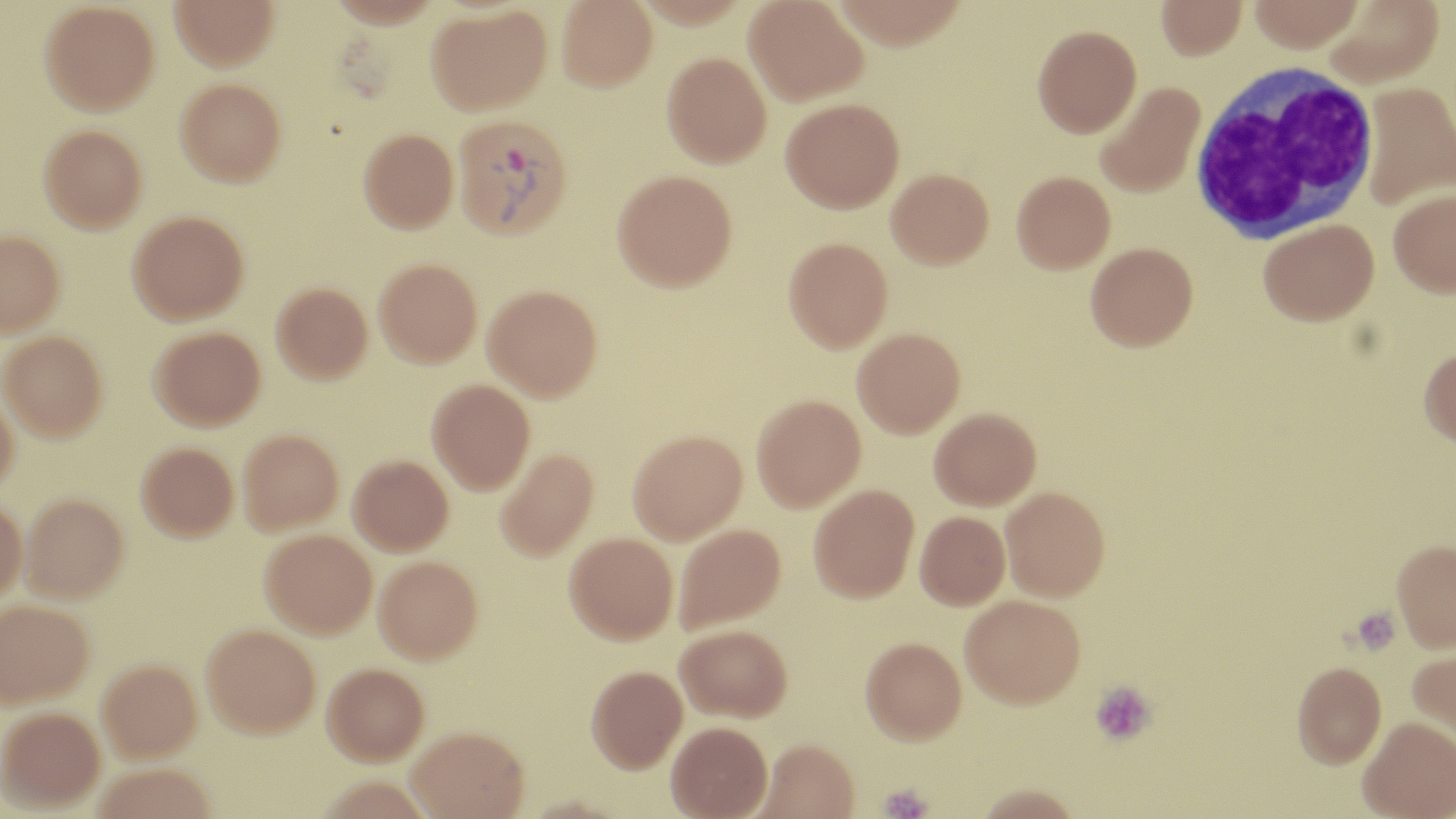
Plasmodium vivax-infected red blood cell locations = approximate bounding boxes as named x1/y1/x2/y2 corners in pixels: (x1=452, y1=113, x2=573, y2=240)
slide-level diagnosis = Plasmodium vivax
magnification = 1000x
platelet locations = approximate bounding boxes as named x1/y1/x2/y2 corners in pixels: (x1=1350, y1=607, x2=1402, y2=655), (x1=1089, y1=680, x2=1157, y2=746), (x1=878, y1=783, x2=933, y2=819)
white blood cell locations = approximate bounding boxes as named x1/y1/x2/y2 corners in pixels: (x1=1190, y1=63, x2=1380, y2=245)
field of view = single
preparation = thin blood film
uninfected red blood cell locations = approximate bounding boxes as named x1/y1/x2/y2 corners in pixels: (x1=170, y1=0, x2=279, y2=70), (x1=556, y1=0, x2=658, y2=91), (x1=744, y1=0, x2=868, y2=105), (x1=1249, y1=0, x2=1364, y2=53), (x1=1322, y1=0, x2=1443, y2=87), (x1=1155, y1=1, x2=1247, y2=61), (x1=40, y1=2, x2=160, y2=115), (x1=426, y1=5, x2=552, y2=115), (x1=1032, y1=25, x2=1141, y2=137), (x1=662, y1=53, x2=771, y2=168), (x1=175, y1=77, x2=286, y2=186), (x1=1093, y1=81, x2=1205, y2=198), (x1=1359, y1=83, x2=1456, y2=210), (x1=781, y1=98, x2=904, y2=213), (x1=39, y1=124, x2=147, y2=232), (x1=358, y1=128, x2=458, y2=233), (x1=886, y1=168, x2=994, y2=268), (x1=612, y1=170, x2=737, y2=291), (x1=1012, y1=171, x2=1115, y2=273), (x1=1388, y1=189, x2=1456, y2=297), (x1=127, y1=211, x2=249, y2=324), (x1=1258, y1=218, x2=1378, y2=325), (x1=0, y1=229, x2=64, y2=337), (x1=783, y1=236, x2=893, y2=352), (x1=1085, y1=241, x2=1198, y2=351), (x1=374, y1=259, x2=482, y2=367), (x1=272, y1=283, x2=372, y2=383), (x1=482, y1=285, x2=602, y2=400), (x1=150, y1=326, x2=266, y2=431), (x1=852, y1=327, x2=965, y2=437), (x1=1, y1=330, x2=107, y2=441), (x1=1418, y1=346, x2=1456, y2=448), (x1=427, y1=379, x2=535, y2=494), (x1=0, y1=387, x2=18, y2=492), (x1=751, y1=394, x2=865, y2=512), (x1=929, y1=408, x2=1041, y2=509), (x1=238, y1=429, x2=343, y2=533), (x1=628, y1=429, x2=747, y2=543), (x1=136, y1=442, x2=238, y2=541), (x1=495, y1=447, x2=598, y2=560), (x1=348, y1=454, x2=453, y2=554), (x1=809, y1=484, x2=919, y2=602), (x1=1000, y1=486, x2=1110, y2=600), (x1=19, y1=492, x2=129, y2=602), (x1=0, y1=496, x2=26, y2=605), (x1=915, y1=511, x2=1010, y2=610), (x1=673, y1=523, x2=786, y2=633), (x1=260, y1=529, x2=377, y2=637), (x1=564, y1=531, x2=678, y2=643), (x1=1392, y1=540, x2=1456, y2=653), (x1=374, y1=555, x2=483, y2=663), (x1=961, y1=595, x2=1085, y2=708), (x1=0, y1=598, x2=93, y2=707), (x1=202, y1=624, x2=321, y2=737), (x1=676, y1=624, x2=792, y2=721), (x1=861, y1=636, x2=967, y2=744), (x1=1408, y1=646, x2=1456, y2=753), (x1=97, y1=659, x2=202, y2=762), (x1=1292, y1=662, x2=1387, y2=770), (x1=322, y1=663, x2=429, y2=764), (x1=586, y1=665, x2=687, y2=772), (x1=0, y1=707, x2=105, y2=811), (x1=1358, y1=719, x2=1456, y2=819), (x1=666, y1=721, x2=772, y2=818), (x1=407, y1=725, x2=529, y2=818), (x1=755, y1=739, x2=861, y2=819), (x1=93, y1=763, x2=216, y2=819), (x1=970, y1=784, x2=1085, y2=818)
stain = May-Grünwald-Giemsa
image size = 1456×819 pixels
modality = optical microscopy